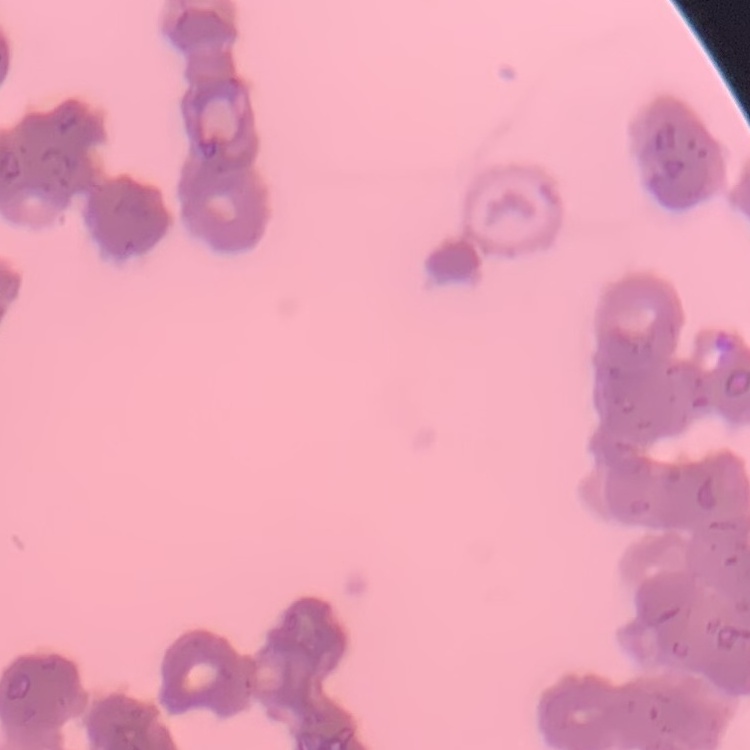

red blood cell morphology = rouleaux formation
preparation = thin blood smear
stain = Field's or Giemsa
image type = square crop of a larger photomicrograph